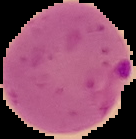

image_type: segmented cell region on a black background
preparation: thin blood film
image_size: 136×139 pixels
result: malaria parasites identified